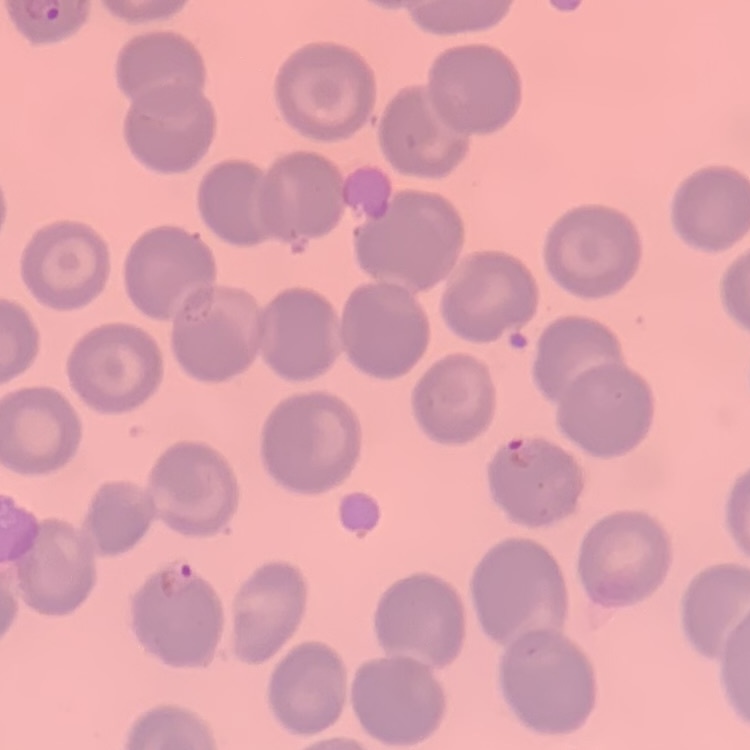 The erythrocytes show no rouleaux formation. Stained with either Field's or Giemsa. Square crop of a larger photomicrograph. Thin blood smear.